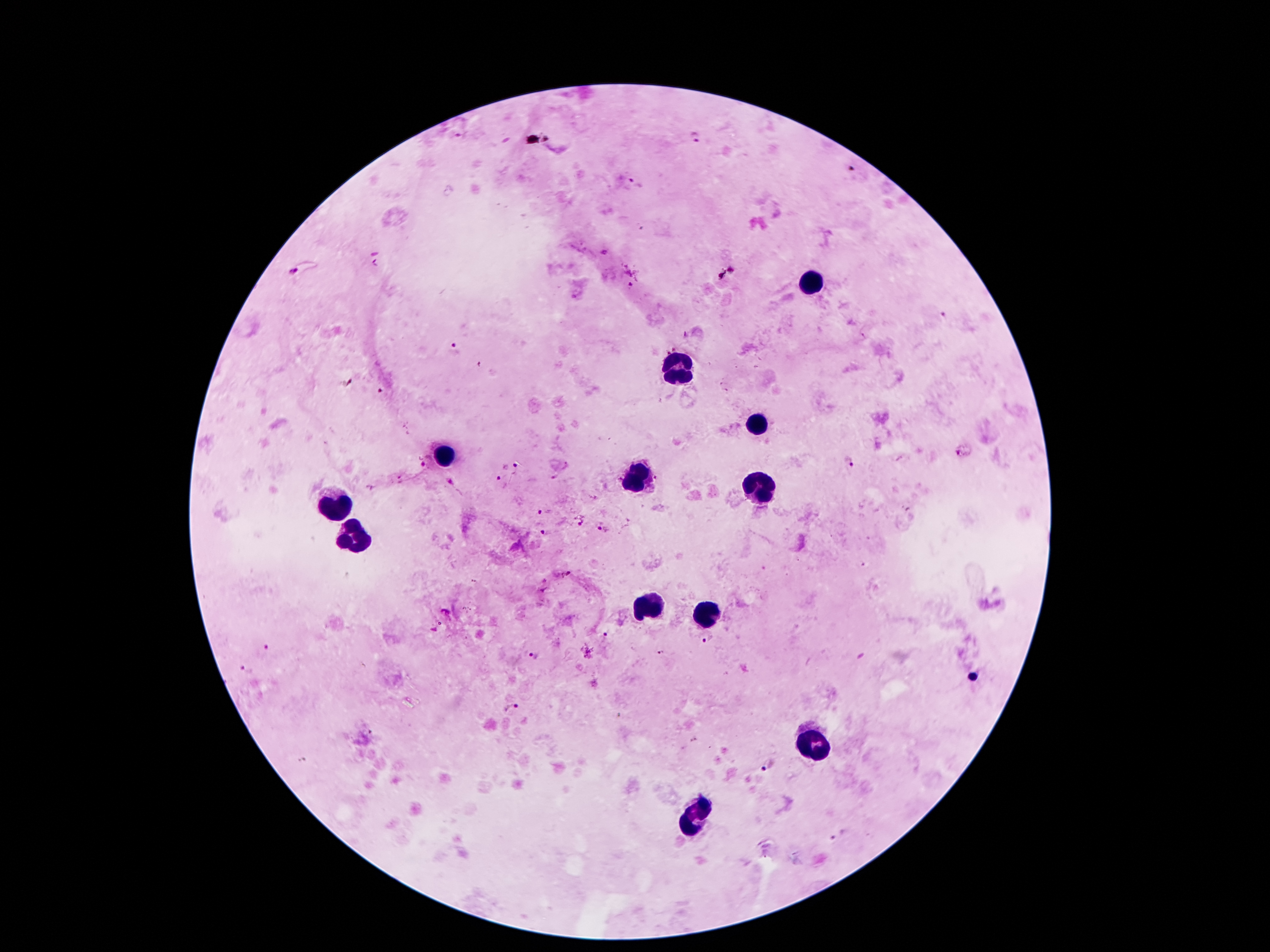 Approximate object centers, in pixels from the top-left corner. Leukocyte locations: (x=811, y=283), (x=684, y=370), (x=759, y=421), (x=446, y=452), (x=637, y=483), (x=757, y=489), (x=337, y=508), (x=353, y=542), (x=643, y=605), (x=707, y=620), (x=818, y=745), (x=693, y=817). Malaria parasite locations: (x=698, y=138), (x=854, y=169), (x=639, y=183), (x=293, y=270), (x=631, y=286), (x=942, y=314), (x=456, y=348), (x=960, y=454), (x=428, y=461), (x=849, y=462), (x=517, y=466), (x=499, y=477), (x=540, y=512), (x=578, y=525), (x=599, y=528), (x=543, y=532), (x=604, y=637), (x=710, y=639), (x=268, y=648), (x=661, y=653), (x=533, y=655), (x=246, y=670), (x=511, y=708), (x=767, y=765), (x=839, y=836). Thick blood smear. One field from this slide. 100x magnification. Giemsa stain. Smartphone photograph taken through the microscope eyepiece. Patient malaria status: positive for Plasmodium falciparum. Image is 1270×952 pixels.